Locate and identify every blood parasite.
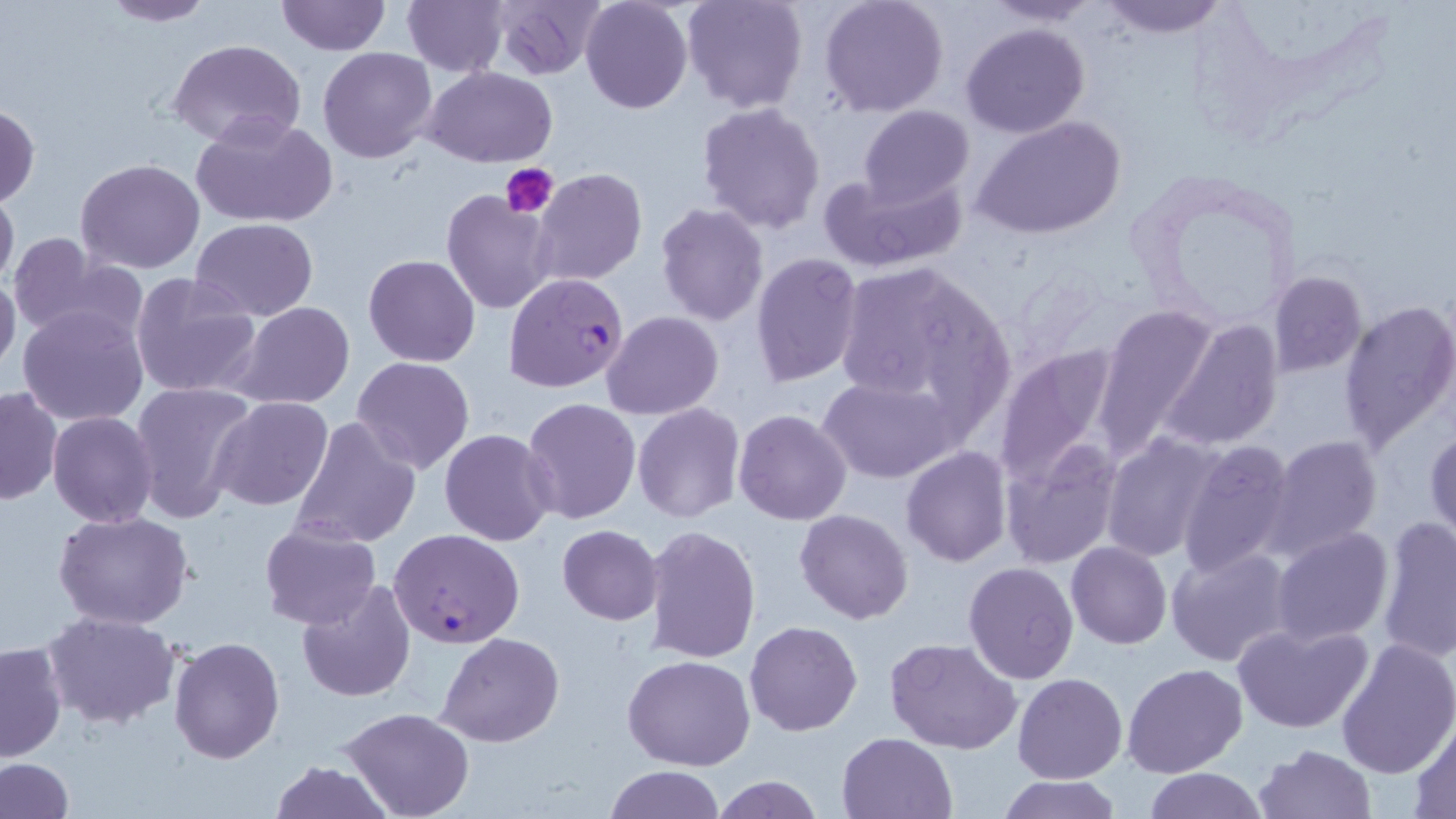
Approximate bounding boxes as (x1, y1, x2, y2) in pixels.
Plasmodium falciparum-infected red blood cells: (504, 272, 630, 394), (388, 528, 526, 647).
No Plasmodium ovale, Plasmodium malariae, Plasmodium vivax, Babesia divergens, or Trypanosoma brucei observed.

Summary:
  - Platelet locations: (503, 163, 560, 218)
  - Uninfected red blood cell locations: (97, 0, 218, 27), (276, 0, 388, 56), (402, 0, 510, 76), (487, 0, 608, 81), (580, 0, 693, 114), (681, 0, 808, 114), (819, 0, 949, 118), (982, 0, 1105, 26), (1095, 0, 1231, 38), (959, 21, 1090, 138), (169, 39, 306, 149), (317, 46, 439, 164), (425, 66, 557, 166), (695, 102, 826, 235), (0, 104, 40, 207), (859, 105, 974, 206), (191, 113, 337, 227), (972, 115, 1126, 242), (75, 159, 205, 274), (533, 169, 648, 288), (818, 169, 970, 273), (0, 188, 18, 293), (440, 189, 558, 314), (654, 203, 769, 326), (191, 218, 320, 319), (7, 232, 122, 340), (750, 252, 864, 388), (363, 255, 482, 367), (831, 261, 1012, 425), (130, 270, 261, 401), (0, 271, 21, 378), (1267, 271, 1367, 377), (1339, 299, 1456, 450), (231, 301, 356, 410), (1093, 305, 1219, 455), (17, 306, 151, 427), (602, 311, 724, 419), (1160, 316, 1284, 453), (994, 344, 1122, 490), (352, 356, 474, 474), (816, 374, 958, 483), (129, 380, 257, 521), (1, 384, 63, 506), (209, 396, 334, 512), (520, 396, 642, 525), (633, 403, 744, 523), (734, 409, 853, 526), (48, 411, 159, 527), (291, 417, 421, 550), (1426, 424, 1456, 547), (439, 429, 558, 546), (1101, 433, 1225, 562), (1267, 435, 1384, 556), (1000, 439, 1122, 569), (1174, 439, 1295, 576), (901, 446, 1012, 567), (52, 509, 195, 630), (794, 509, 915, 624), (1375, 515, 1456, 662), (259, 523, 382, 631), (557, 524, 663, 625), (643, 525, 762, 666), (1271, 527, 1394, 646), (1066, 542, 1171, 650), (1166, 546, 1295, 668), (962, 560, 1080, 685), (296, 581, 417, 701), (42, 610, 182, 729), (745, 621, 862, 736), (1233, 621, 1374, 734), (437, 632, 565, 747), (168, 634, 286, 763), (886, 637, 1023, 753), (1336, 638, 1456, 778), (0, 641, 67, 763), (622, 655, 755, 771), (1121, 662, 1248, 778), (1012, 672, 1127, 783), (339, 707, 475, 818), (1408, 712, 1456, 816), (836, 731, 956, 818), (1252, 744, 1378, 819), (0, 758, 76, 819), (266, 760, 397, 818), (601, 766, 727, 819), (1143, 768, 1268, 819), (708, 776, 827, 818), (995, 776, 1124, 818)
  - Slide-level diagnosis: Plasmodium falciparum
  - Magnification: 1000x
  - Image size: 1456×819 pixels
  - Field of view: single
  - Modality: light microscopy
  - Preparation: thin blood film
  - Stain: May-Grünwald-Giemsa